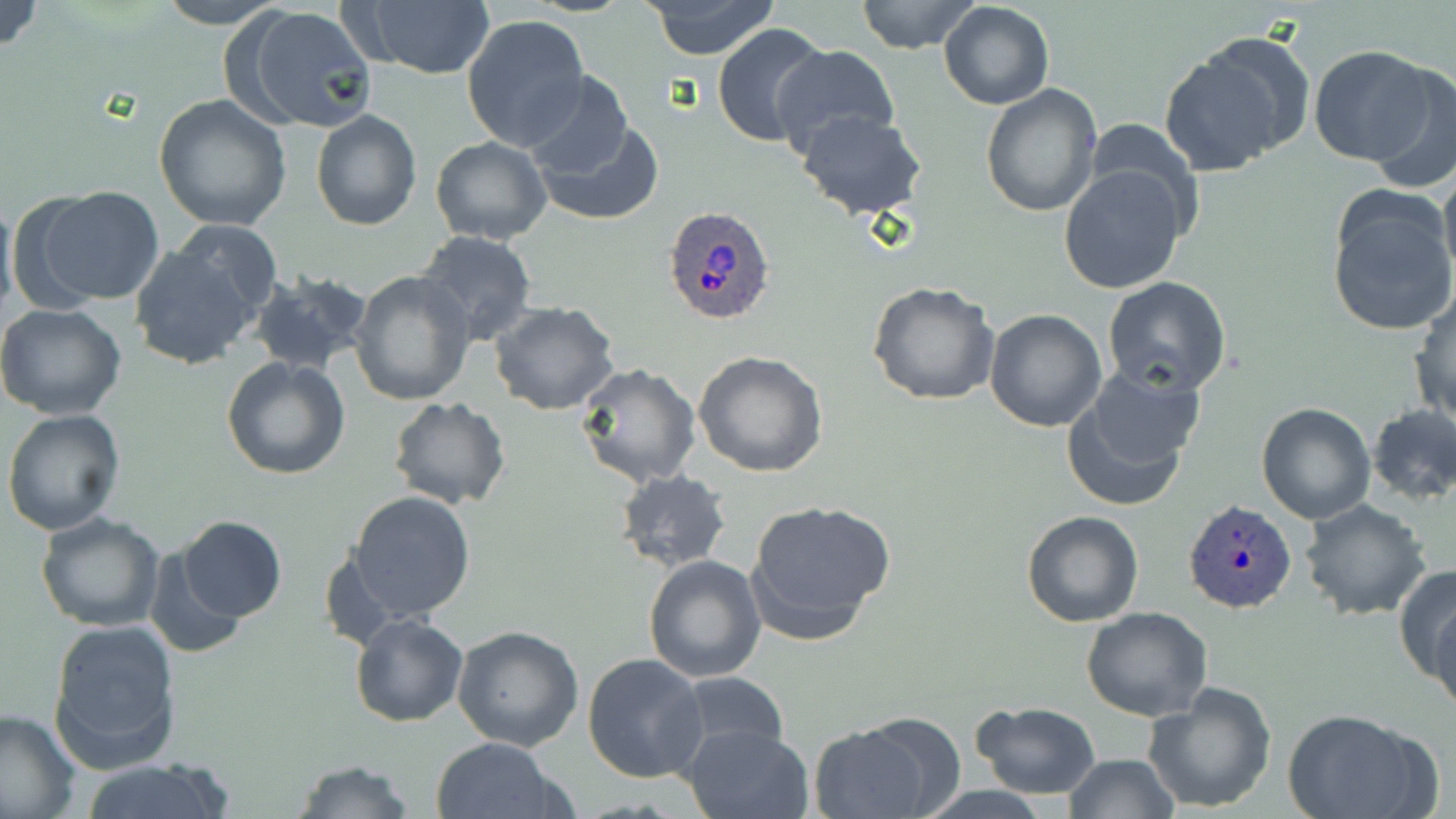

Approximate bounding boxes as (x1,y1)-(x2,y2) corner pairs in pixels. Plasmodium ovale-infected red blood cell locations: (662,204)-(778,325), (1182,500)-(1297,613). Uninfected red blood cell locations: (0,0)-(45,54), (154,0)-(284,28), (643,0)-(780,59), (857,0)-(979,54), (350,1)-(497,80), (938,1)-(1054,110), (237,7)-(377,133), (462,14)-(589,150), (711,22)-(832,147), (770,44)-(901,158), (1155,45)-(1298,177), (1310,46)-(1441,165), (1364,64)-(1456,194), (522,70)-(636,181), (981,81)-(1104,217), (154,94)-(293,231), (310,109)-(422,230), (796,111)-(928,219), (531,116)-(663,224), (429,136)-(552,245), (1438,161)-(1456,290), (1060,162)-(1190,295), (22,184)-(164,306), (1326,189)-(1456,338), (0,191)-(18,325), (164,221)-(285,324), (414,231)-(537,345), (129,242)-(262,371), (348,270)-(477,408), (248,271)-(373,376), (1101,275)-(1232,396), (867,282)-(1001,406), (1408,289)-(1456,425), (489,301)-(621,416), (0,303)-(128,419), (985,308)-(1107,431), (693,350)-(829,479), (221,357)-(351,480), (575,362)-(702,488), (1060,367)-(1204,511), (388,397)-(511,510), (1256,402)-(1376,523), (1366,402)-(1456,507), (2,409)-(126,535), (612,469)-(733,571), (348,490)-(478,623), (744,498)-(897,643), (1299,498)-(1431,620), (1021,509)-(1144,627), (35,510)-(166,630), (177,516)-(287,623), (145,545)-(251,659), (643,554)-(766,681), (1397,565)-(1455,697), (1428,591)-(1456,723), (1080,606)-(1213,721), (351,614)-(468,727), (47,618)-(182,773), (452,626)-(585,751), (582,653)-(709,782), (672,673)-(792,760), (1143,682)-(1277,813), (971,701)-(1101,798), (0,708)-(81,818), (1286,709)-(1434,819), (810,716)-(948,819), (685,724)-(811,819), (429,737)-(559,819), (1063,753)-(1181,818), (78,758)-(238,819), (293,760)-(416,818). Slide-level diagnosis: Plasmodium ovale. Image is 1456×819 pixels. 1000x magnification. One field of a larger specimen. Thin blood film. Optical microscopy. May-Grünwald-Giemsa-stained preparation.